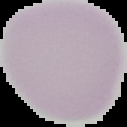
Image is 127×127 pixels. Result: no Plasmodium parasites detected. From a thin blood film. Cell region segmented out of the field of view; the surrounding area is masked to black.